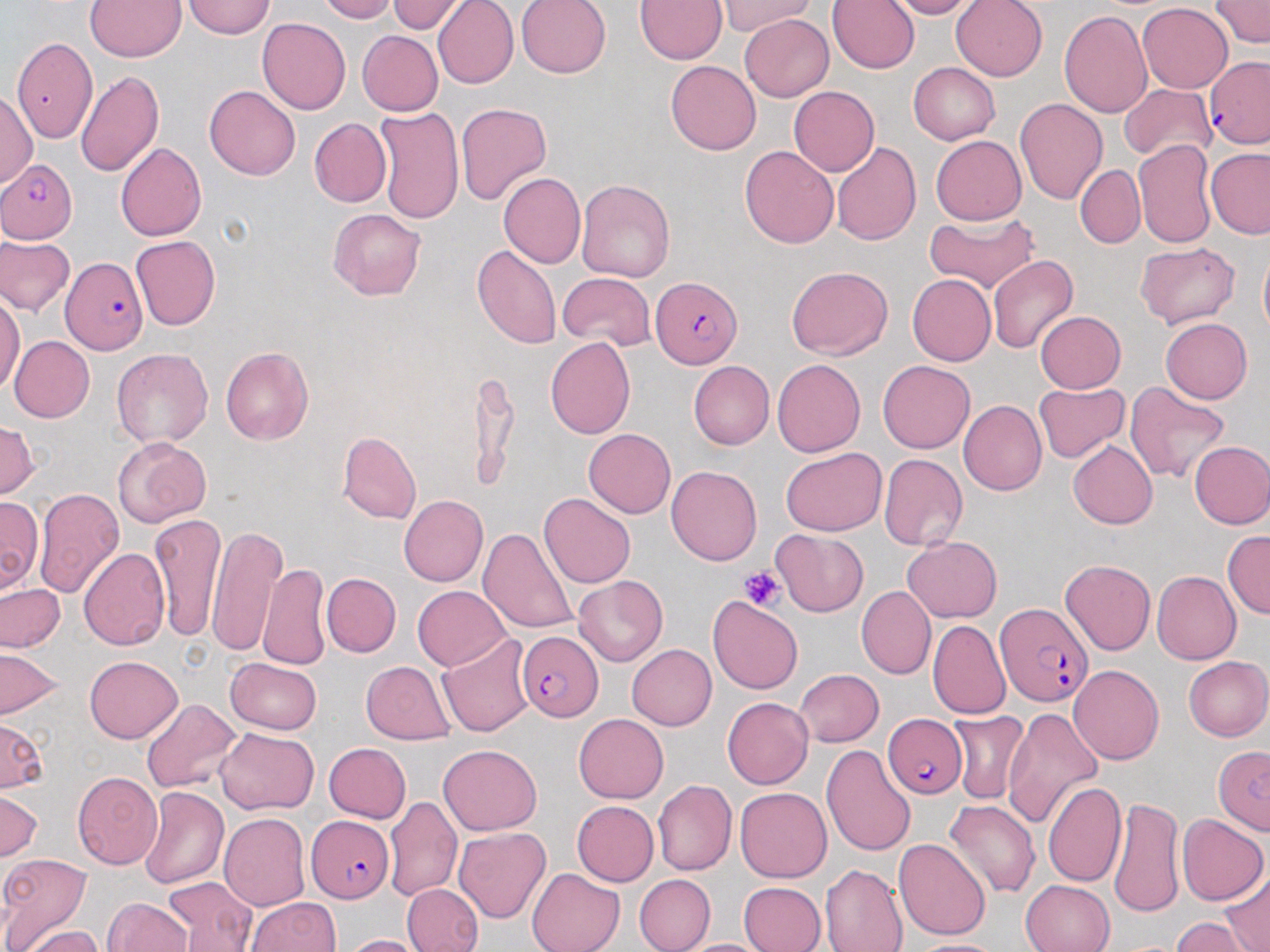

Summary:
  - Coordinate format: approximate bounding boxes as named x1/y1/x2/y2 corners in pixels
  - Plasmodium falciparum-infected red blood cell locations: (x1=1205, y1=56, x2=1270, y2=148), (x1=0, y1=159, x2=79, y2=244), (x1=61, y1=258, x2=147, y2=354), (x1=650, y1=276, x2=743, y2=367), (x1=997, y1=601, x2=1092, y2=707), (x1=517, y1=631, x2=604, y2=721), (x1=887, y1=714, x2=966, y2=798), (x1=1213, y1=747, x2=1270, y2=835), (x1=306, y1=815, x2=394, y2=903)
  - Uninfected red blood cell locations: (x1=85, y1=0, x2=186, y2=61), (x1=182, y1=0, x2=274, y2=39), (x1=317, y1=0, x2=396, y2=23), (x1=433, y1=0, x2=519, y2=88), (x1=516, y1=0, x2=612, y2=79), (x1=636, y1=0, x2=727, y2=64), (x1=827, y1=0, x2=920, y2=73), (x1=885, y1=0, x2=976, y2=19), (x1=950, y1=0, x2=1048, y2=81), (x1=1208, y1=0, x2=1270, y2=47), (x1=388, y1=1, x2=467, y2=34), (x1=721, y1=2, x2=815, y2=35), (x1=1137, y1=2, x2=1233, y2=93), (x1=1058, y1=10, x2=1154, y2=119), (x1=740, y1=15, x2=834, y2=102), (x1=258, y1=17, x2=351, y2=113), (x1=357, y1=31, x2=444, y2=116), (x1=11, y1=37, x2=97, y2=142), (x1=665, y1=60, x2=761, y2=155), (x1=909, y1=62, x2=1000, y2=145), (x1=75, y1=70, x2=162, y2=176), (x1=204, y1=84, x2=300, y2=179), (x1=788, y1=85, x2=880, y2=176), (x1=1119, y1=85, x2=1215, y2=162), (x1=0, y1=90, x2=37, y2=189), (x1=1014, y1=99, x2=1107, y2=205), (x1=456, y1=102, x2=552, y2=205), (x1=374, y1=106, x2=464, y2=224), (x1=309, y1=117, x2=392, y2=208), (x1=931, y1=135, x2=1026, y2=224), (x1=1132, y1=138, x2=1217, y2=248), (x1=115, y1=143, x2=207, y2=241), (x1=831, y1=143, x2=921, y2=247), (x1=740, y1=146, x2=838, y2=248), (x1=1205, y1=148, x2=1270, y2=240), (x1=1075, y1=165, x2=1144, y2=248), (x1=498, y1=172, x2=586, y2=268), (x1=575, y1=178, x2=676, y2=283), (x1=328, y1=208, x2=426, y2=299), (x1=923, y1=213, x2=1039, y2=293), (x1=1, y1=236, x2=73, y2=314), (x1=130, y1=236, x2=221, y2=330), (x1=1135, y1=242, x2=1241, y2=329), (x1=473, y1=244, x2=559, y2=349), (x1=1259, y1=245, x2=1270, y2=342), (x1=988, y1=254, x2=1078, y2=353), (x1=785, y1=266, x2=892, y2=359), (x1=558, y1=273, x2=655, y2=349), (x1=907, y1=273, x2=995, y2=367), (x1=892, y1=278, x2=982, y2=456), (x1=0, y1=292, x2=25, y2=395), (x1=1036, y1=311, x2=1125, y2=394), (x1=1160, y1=318, x2=1252, y2=403), (x1=9, y1=335, x2=94, y2=422), (x1=544, y1=337, x2=637, y2=438), (x1=220, y1=346, x2=313, y2=444), (x1=111, y1=348, x2=212, y2=448), (x1=772, y1=359, x2=865, y2=457), (x1=688, y1=361, x2=774, y2=450), (x1=878, y1=361, x2=975, y2=453), (x1=467, y1=374, x2=518, y2=491), (x1=1124, y1=381, x2=1230, y2=483), (x1=1034, y1=382, x2=1129, y2=463), (x1=958, y1=399, x2=1047, y2=496), (x1=0, y1=417, x2=38, y2=499), (x1=583, y1=429, x2=676, y2=518), (x1=338, y1=432, x2=420, y2=524), (x1=113, y1=436, x2=211, y2=526), (x1=1069, y1=440, x2=1158, y2=529), (x1=1189, y1=440, x2=1270, y2=529), (x1=780, y1=448, x2=887, y2=535), (x1=878, y1=454, x2=968, y2=551), (x1=666, y1=465, x2=762, y2=565), (x1=33, y1=487, x2=127, y2=598), (x1=539, y1=492, x2=635, y2=587), (x1=398, y1=495, x2=487, y2=585), (x1=0, y1=497, x2=43, y2=594), (x1=150, y1=511, x2=225, y2=640), (x1=205, y1=525, x2=286, y2=658), (x1=479, y1=528, x2=579, y2=636), (x1=772, y1=530, x2=869, y2=616), (x1=1222, y1=530, x2=1269, y2=619), (x1=901, y1=537, x2=1002, y2=622), (x1=78, y1=548, x2=170, y2=650), (x1=1060, y1=559, x2=1155, y2=654), (x1=258, y1=563, x2=330, y2=671), (x1=1151, y1=570, x2=1241, y2=665), (x1=320, y1=573, x2=401, y2=657), (x1=573, y1=576, x2=667, y2=666), (x1=0, y1=582, x2=65, y2=653), (x1=856, y1=585, x2=935, y2=679), (x1=412, y1=586, x2=513, y2=670), (x1=708, y1=595, x2=803, y2=695), (x1=928, y1=619, x2=1011, y2=720), (x1=437, y1=633, x2=535, y2=737), (x1=627, y1=644, x2=717, y2=730), (x1=0, y1=648, x2=65, y2=720), (x1=84, y1=656, x2=183, y2=744), (x1=1183, y1=656, x2=1270, y2=740), (x1=224, y1=657, x2=320, y2=734), (x1=361, y1=661, x2=455, y2=744), (x1=1069, y1=665, x2=1163, y2=765), (x1=793, y1=670, x2=883, y2=747), (x1=721, y1=697, x2=813, y2=789), (x1=140, y1=698, x2=242, y2=793), (x1=1003, y1=707, x2=1102, y2=828), (x1=947, y1=710, x2=1031, y2=804), (x1=574, y1=713, x2=668, y2=803), (x1=0, y1=719, x2=49, y2=793), (x1=215, y1=727, x2=317, y2=815), (x1=324, y1=743, x2=411, y2=822), (x1=438, y1=744, x2=541, y2=835), (x1=820, y1=744, x2=916, y2=856), (x1=72, y1=771, x2=162, y2=870), (x1=653, y1=780, x2=737, y2=877), (x1=1042, y1=781, x2=1126, y2=888), (x1=139, y1=786, x2=228, y2=889), (x1=734, y1=787, x2=831, y2=882), (x1=0, y1=789, x2=43, y2=862), (x1=383, y1=796, x2=463, y2=901), (x1=1108, y1=796, x2=1184, y2=919), (x1=944, y1=800, x2=1041, y2=899), (x1=571, y1=801, x2=659, y2=886), (x1=219, y1=812, x2=311, y2=910), (x1=1177, y1=813, x2=1268, y2=905), (x1=453, y1=828, x2=551, y2=925), (x1=894, y1=838, x2=990, y2=940), (x1=0, y1=852, x2=92, y2=949), (x1=821, y1=865, x2=907, y2=952), (x1=527, y1=869, x2=624, y2=952), (x1=1222, y1=870, x2=1270, y2=952), (x1=634, y1=875, x2=714, y2=952), (x1=163, y1=877, x2=258, y2=951), (x1=1020, y1=879, x2=1115, y2=952), (x1=739, y1=881, x2=827, y2=952), (x1=401, y1=882, x2=484, y2=952), (x1=103, y1=897, x2=192, y2=952), (x1=245, y1=898, x2=340, y2=951), (x1=9, y1=907, x2=100, y2=950), (x1=1170, y1=917, x2=1260, y2=952), (x1=22, y1=926, x2=105, y2=952), (x1=340, y1=934, x2=431, y2=952), (x1=675, y1=938, x2=776, y2=951), (x1=907, y1=939, x2=1007, y2=952)
  - Platelet locations: (x1=739, y1=565, x2=786, y2=614)
  - Slide-level diagnosis: Plasmodium falciparum
  - Stain: May-Grünwald-Giemsa
  - Preparation: thin blood film
  - Magnification: 1000x
  - Field of view: one of a larger specimen
  - Modality: optical microscopy
  - Image size: 1270×952 pixels